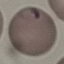
Summary:
  - Malaria status: parasitized
  - Stain: Giemsa
  - Capture: smartphone through the microscope eyepiece
  - Preparation: thin blood film
  - Image type: automatically extracted cell patch, resized to 64 × 64 pixels